Report the malaria status of this cell.
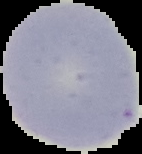
Uninfected.

image size = 142×154 pixels
preparation = thin blood smear
image type = segmented cell region on a black background